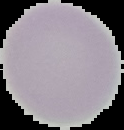

image type = cell region segmented out of the field of view; surrounding area masked to black
image size = 124×130 pixels
preparation = thin blood smear
result = negative for malaria parasites